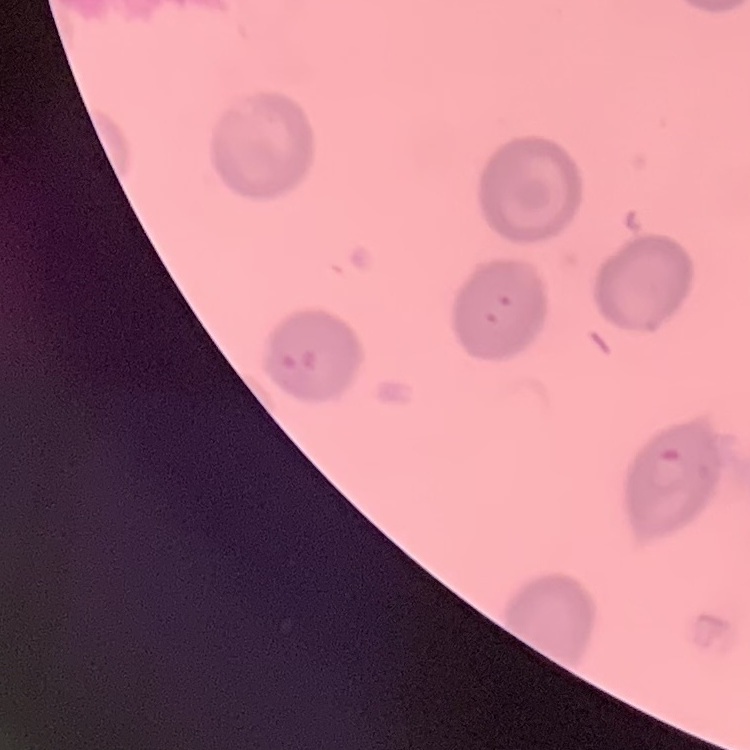

Summary:
  - Red blood cell morphology: no rouleaux formation
  - Stain: Field's or Giemsa
  - Preparation: thin blood film
  - Image type: square crop of a larger photomicrograph